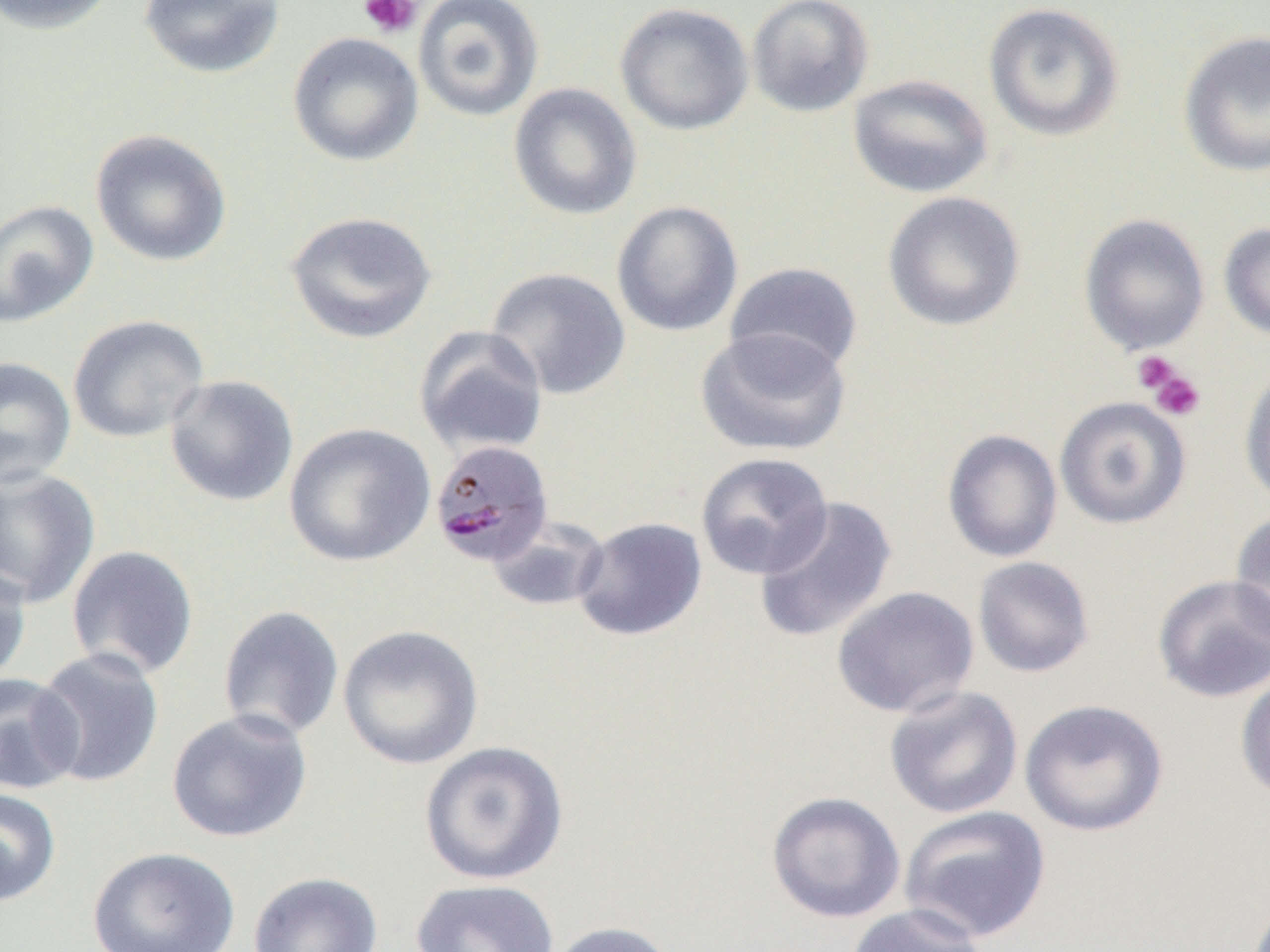
Summary:
  - Coordinate format: approximate bounding boxes as (x1, y1, x2, y2) in pixels
  - Uninfected red blood cell locations: (0, 0, 120, 35), (138, 0, 286, 80), (413, 0, 545, 122), (746, 0, 874, 117), (614, 2, 754, 136), (983, 2, 1126, 142), (1177, 30, 1270, 177), (287, 32, 424, 167), (847, 73, 994, 199), (507, 83, 642, 220), (90, 129, 232, 268), (882, 191, 1026, 332), (0, 199, 99, 328), (611, 200, 744, 337), (285, 210, 438, 344), (1078, 213, 1210, 355), (1219, 222, 1270, 341), (724, 261, 864, 376), (486, 267, 631, 401), (67, 315, 209, 444), (413, 326, 550, 458), (695, 327, 852, 458), (0, 357, 77, 488), (1238, 363, 1270, 507), (164, 374, 299, 507), (1054, 396, 1191, 530), (283, 422, 436, 568), (942, 428, 1063, 563), (695, 452, 834, 580), (0, 466, 101, 609), (753, 496, 898, 643), (1229, 510, 1270, 648), (572, 516, 707, 641), (486, 517, 610, 613), (65, 544, 199, 680), (972, 555, 1095, 678), (0, 560, 32, 687), (1152, 574, 1270, 702), (831, 585, 980, 719), (217, 605, 345, 742), (337, 624, 484, 771), (32, 648, 165, 788), (1235, 670, 1270, 804), (0, 673, 82, 795), (884, 685, 1023, 819), (1019, 698, 1169, 837), (166, 708, 313, 843), (418, 740, 571, 885), (0, 786, 61, 907), (765, 791, 906, 923), (899, 805, 1052, 944), (86, 846, 241, 952), (248, 871, 384, 952), (410, 878, 560, 952), (845, 904, 989, 952), (543, 920, 679, 952)
  - Platelet locations: (357, 0, 423, 39), (1132, 350, 1186, 401), (1144, 363, 1206, 422)
  - Plasmodium malariae-infected red blood cell locations: (429, 439, 554, 567)
  - Slide-level diagnosis: Plasmodium malariae
  - Image size: 1270×952 pixels
  - Preparation: thin blood film
  - Magnification: 1000x
  - Modality: optical microscopy
  - Field of view: one of a larger specimen